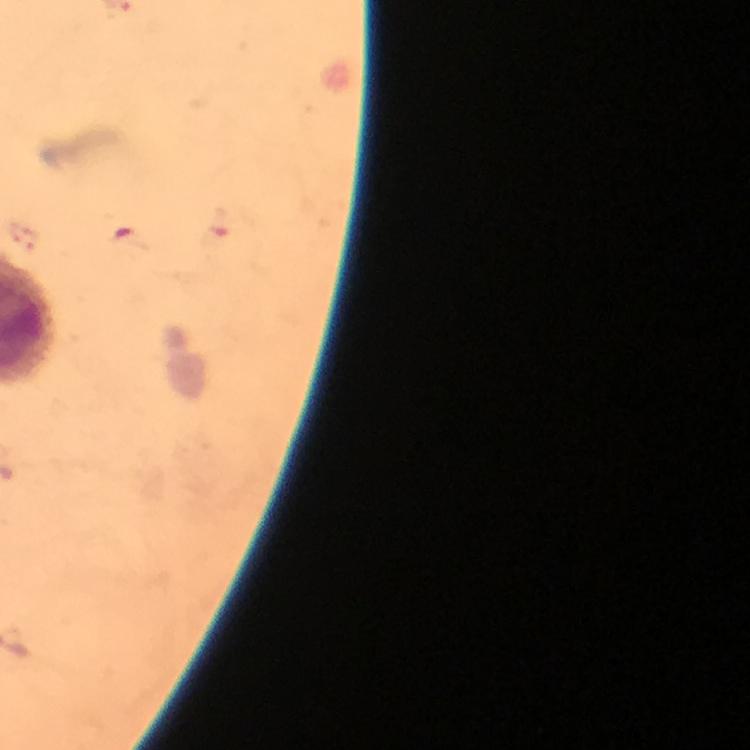

Approximate centers as (x, y) in pixels. Malaria parasite locations: (220, 223). From a diagnostic examination for malaria. Image is 750×750 pixels. Giemsa-stained preparation. 100x magnification. Photographed with a smartphone mounted on the microscope. A crop from one field of view. Thick smear. Immersion oil applied.